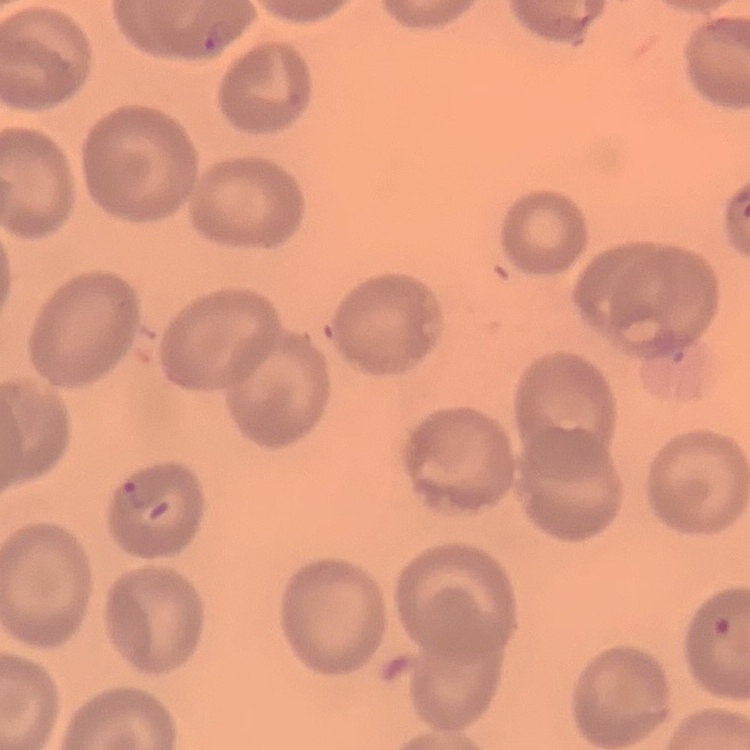 The erythrocytes show no rouleaux formation. Square crop of a larger photomicrograph. Stained with either Field's or Giemsa. Thin blood smear.